Assess this cell for malaria.
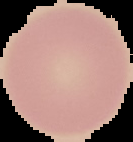

It is uninfected.

The area outside the segmented cell region is set to black. Image is 133×142 pixels. From a thin blood smear.